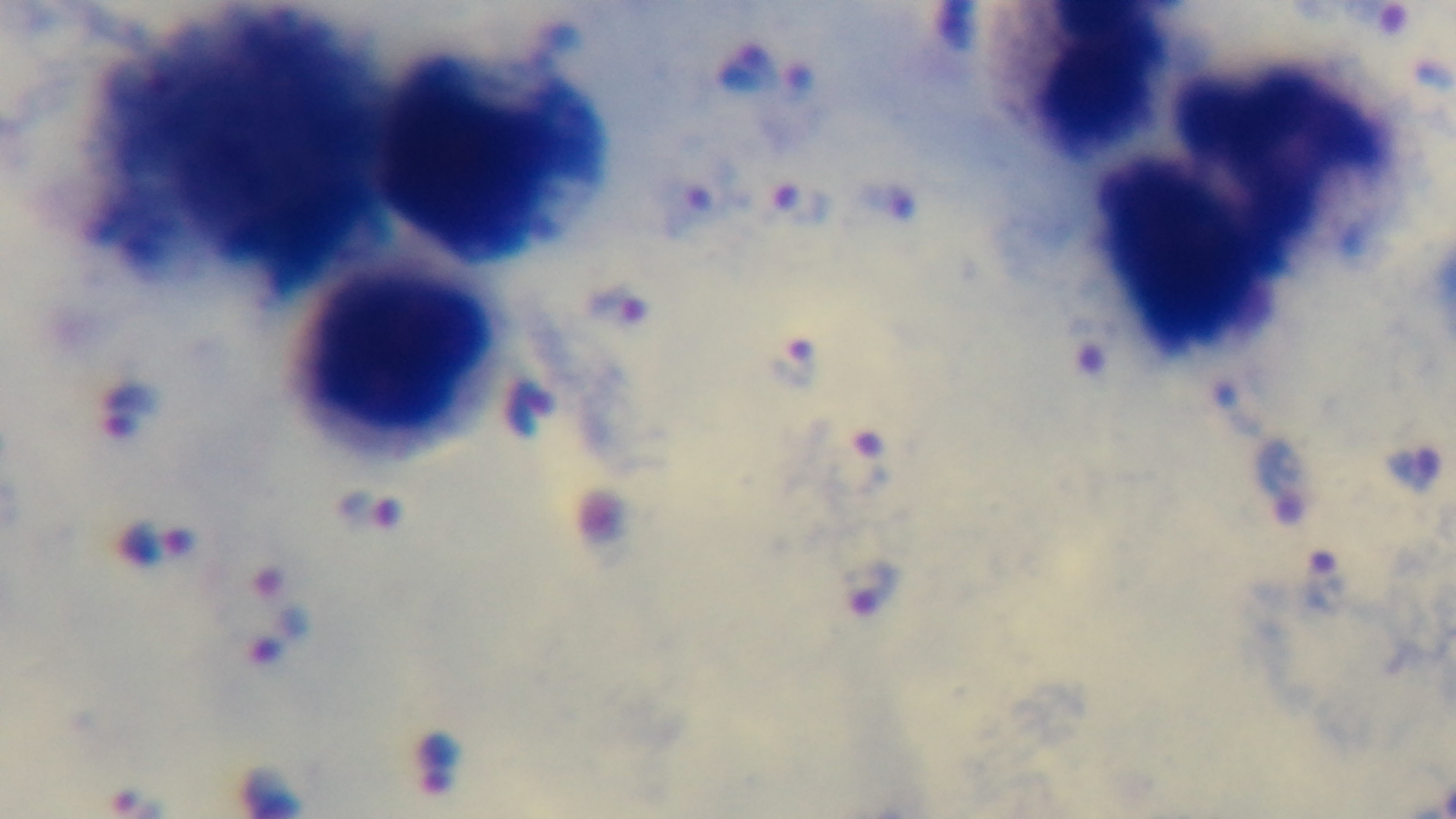
Summary:
  - Stain: Giemsa
  - Malaria status: infected
  - Capture: mounted 4K digital camera
  - Field of view: single
  - Preparation: thick
  - Modality: light microscopy
  - Objective: 100x oil immersion